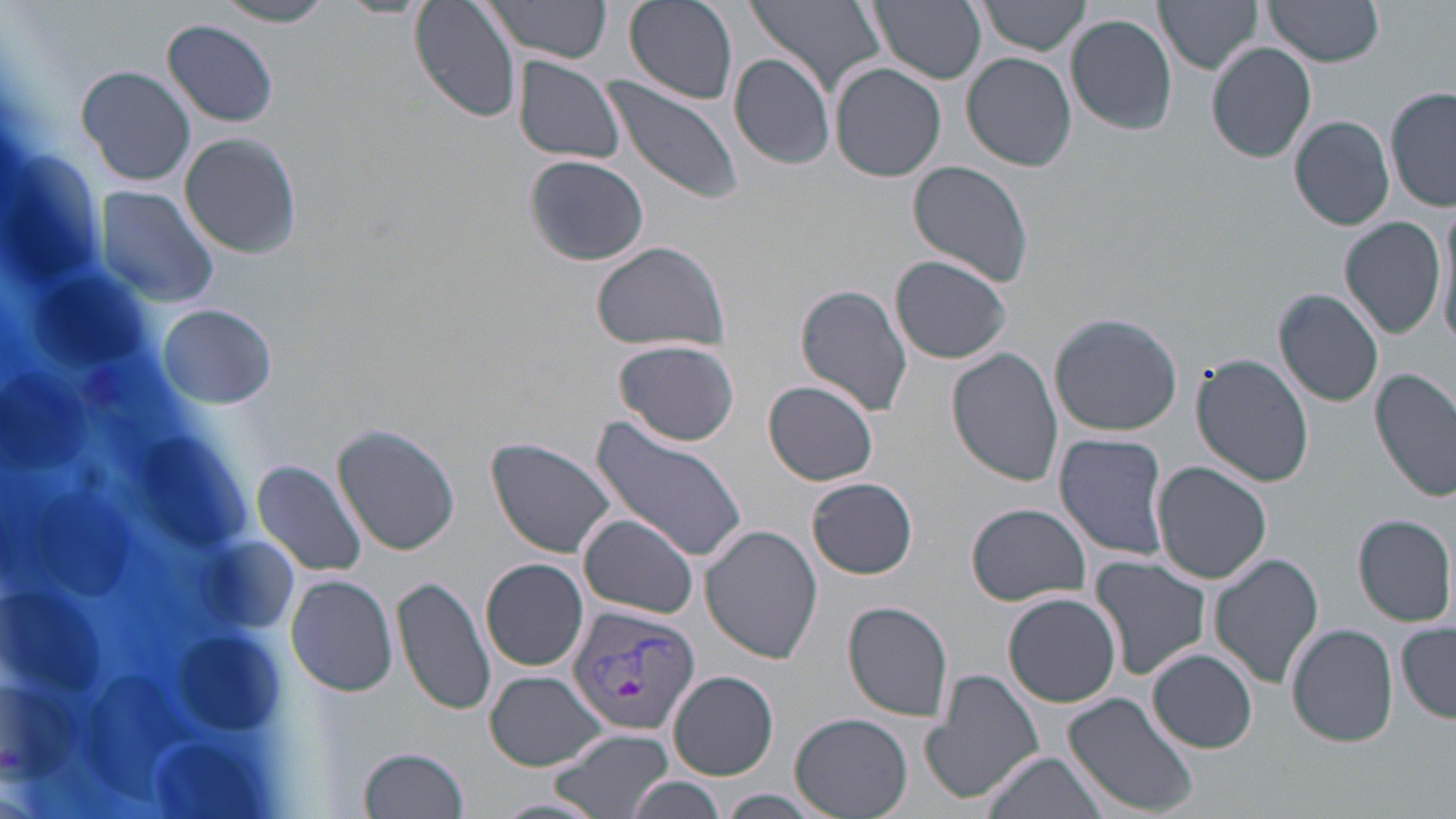
slide-level diagnosis = Plasmodium vivax
stain = May-Grünwald-Giemsa
field of view = one of a larger specimen
image size = 1456×819 pixels
uninfected red blood cell locations = approximate bounding boxes as [x1, y1, x2, y2] in pixels: [410, 0, 521, 123], [479, 0, 613, 64], [626, 0, 739, 104], [746, 0, 884, 98], [865, 0, 986, 84], [977, 0, 1093, 56], [1155, 0, 1265, 74], [1265, 0, 1383, 68], [216, 1, 333, 26], [1064, 14, 1177, 135], [162, 19, 280, 126], [1207, 42, 1317, 163], [729, 53, 837, 170], [962, 53, 1077, 171], [511, 57, 627, 165], [830, 63, 946, 182], [77, 64, 196, 187], [604, 75, 742, 204], [1386, 89, 1456, 211], [1290, 115, 1394, 230], [180, 132, 301, 260], [523, 154, 650, 267], [908, 162, 1035, 286], [91, 184, 221, 311], [1339, 215, 1446, 340], [1436, 216, 1456, 356], [590, 240, 731, 353], [890, 255, 1013, 364], [795, 283, 913, 416], [1274, 287, 1385, 408], [158, 303, 277, 409], [1049, 313, 1182, 436], [614, 339, 740, 446], [948, 349, 1062, 485], [1191, 353, 1312, 486], [1370, 368, 1456, 502], [764, 380, 879, 486], [587, 418, 751, 564], [333, 422, 460, 556], [1054, 432, 1170, 561], [488, 437, 620, 560], [250, 459, 369, 578], [1154, 462, 1272, 585], [809, 477, 917, 579], [965, 503, 1093, 605], [1354, 513, 1454, 626], [578, 514, 701, 618], [701, 525, 823, 664], [1207, 553, 1323, 690], [1091, 555, 1211, 680], [481, 559, 589, 671], [284, 572, 399, 698], [392, 576, 497, 716], [1003, 594, 1120, 708], [843, 599, 953, 720], [1287, 623, 1397, 749], [1397, 623, 1455, 722], [1148, 649, 1259, 752], [919, 667, 1043, 805], [486, 671, 605, 771], [668, 671, 778, 780], [1063, 693, 1199, 818], [790, 713, 913, 819], [548, 727, 675, 819], [358, 746, 469, 819], [980, 749, 1111, 819], [625, 776, 729, 818]
Plasmodium vivax-infected red blood cell locations = approximate bounding boxes as [x1, y1, x2, y2] in pixels: [570, 604, 700, 733]
magnification = 1000x
modality = optical microscopy
white blood cell locations = approximate bounding boxes as [x1, y1, x2, y2] in pixels: [0, 154, 321, 819]
preparation = thin blood smear